Classify the preparation.
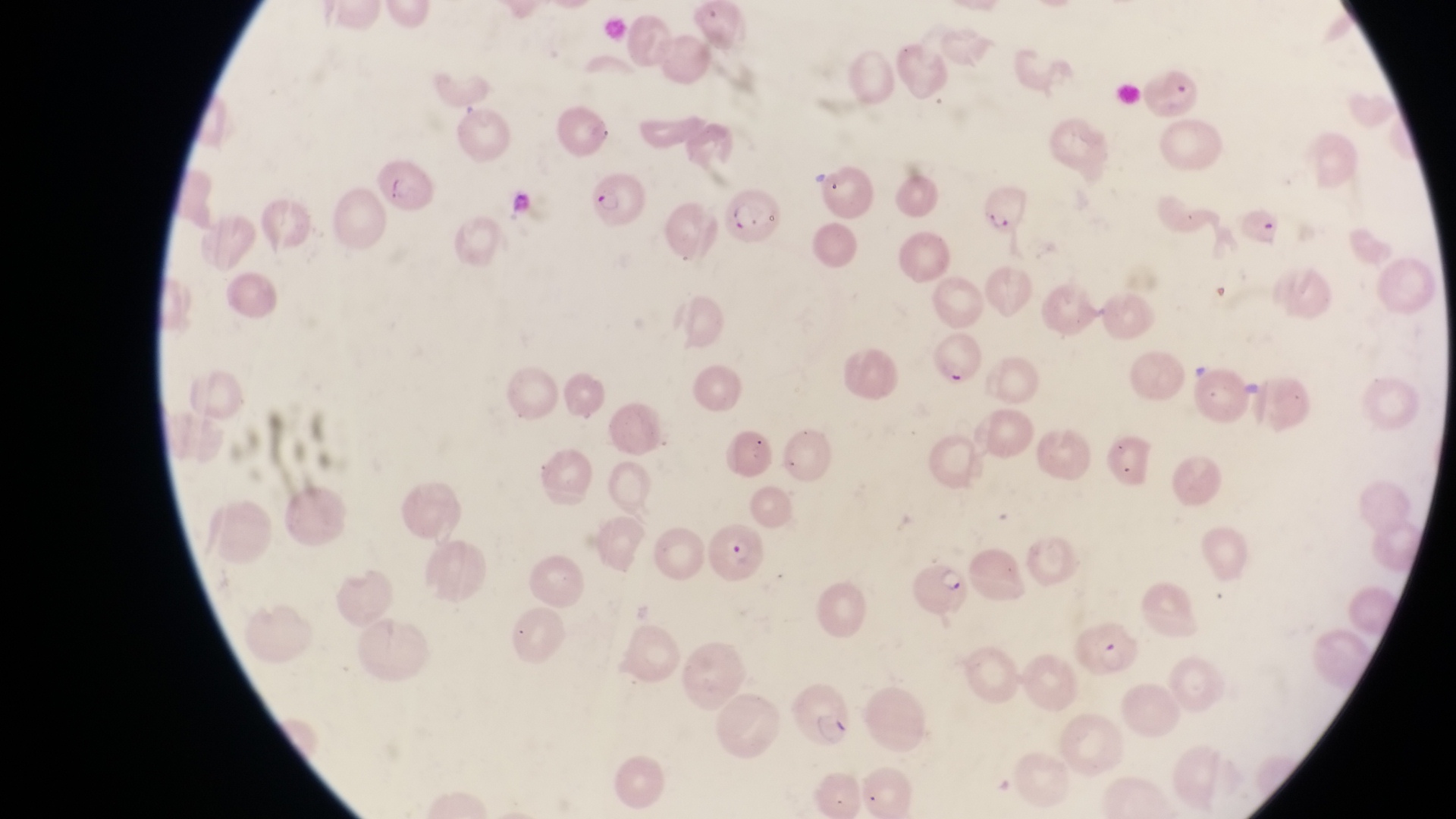
Thin blood smear.

Approximate bounding boxes as {left, top, right, bottom} in pixels. Parasitised red blood cell locations: {1147, 63, 1210, 124}, {377, 165, 436, 220}, {591, 174, 643, 230}, {983, 185, 1035, 238}, {727, 192, 786, 248}, {931, 331, 986, 395}, {710, 522, 774, 585}, {907, 549, 968, 616}, {1076, 618, 1142, 689}, {789, 682, 856, 753}. Sample from Uganda. Captured by a smartphone held over the eyepiece of an Olympus CX-23 microscope. Magnification of 1000x. Single field of view. Image is 1456×819 pixels.